Assess this cell for malaria.
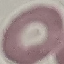

Uninfected.

preparation = thin blood smear
capture = smartphone camera at the microscope eyepiece
image type = cell patch, automatically extracted from a larger field of view and resized to 64 × 64 pixels
stain = Giemsa